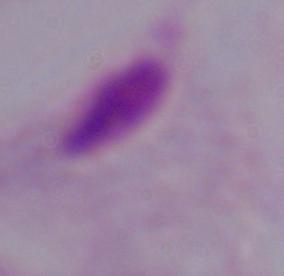 Captured at 1000x magnification. Micrograph. A trichomonad is seen.